Report the malaria status of this cell.
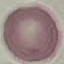

Uninfected.

Acquired by smartphone through the microscope eyepiece. Giemsa-stained preparation. Automatically extracted cell patch, resized to 64 × 64 pixels. Thin blood smear.